State the preparation type.
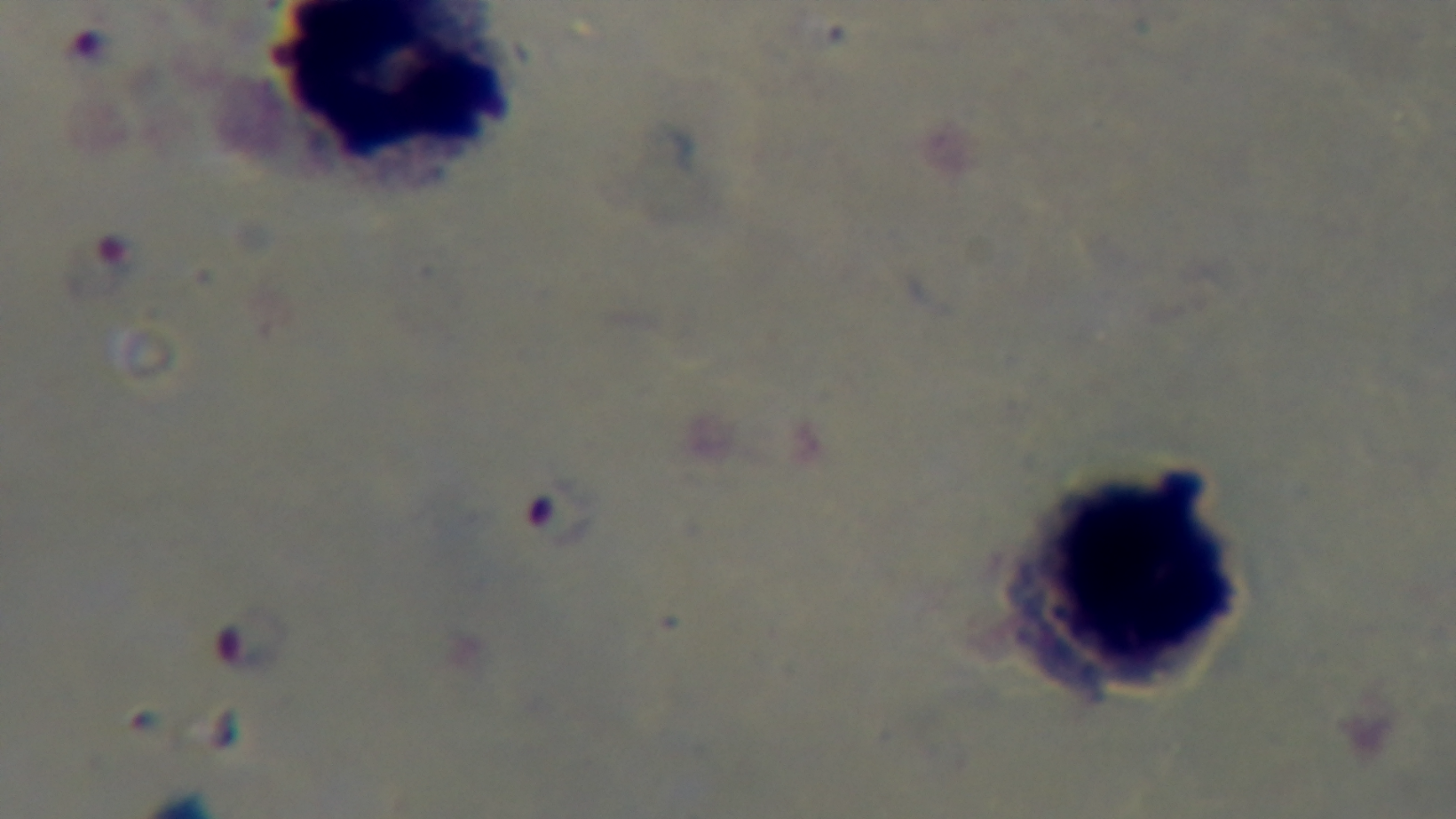

Thick.

Summary:
  - Modality: light microscopy
  - Field of view: one from the slide
  - Malaria status: positive
  - Capture: mounted 4K digital camera
  - Stain: Giemsa
  - Objective: 100x oil immersion